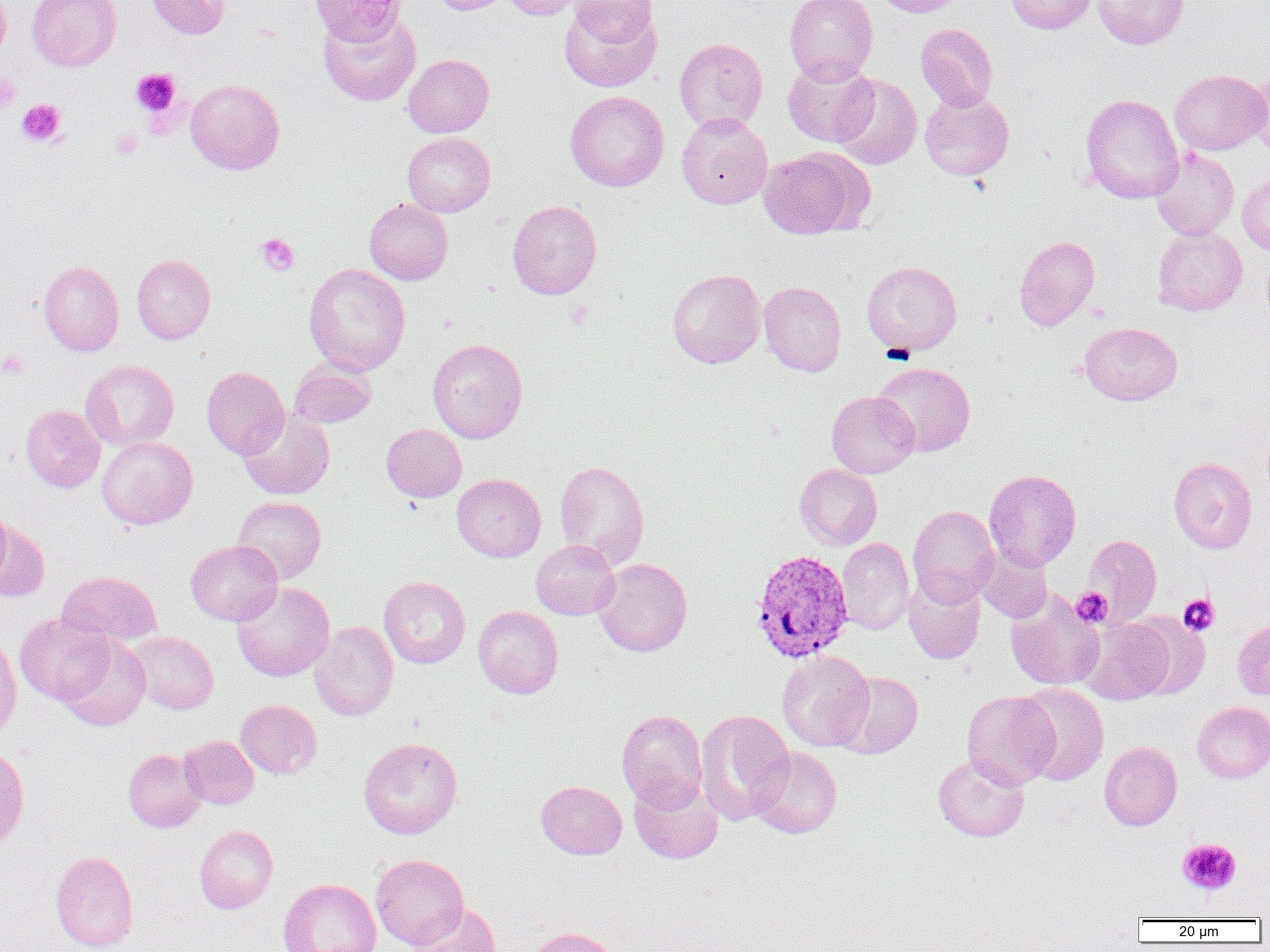

Summary:
  - Coordinate format: approximate bounding boxes as [x1, y1, x2, y2] in pixels
  - Uninfected red blood cell locations: [0, 0, 10, 68], [26, 0, 122, 71], [147, 0, 231, 39], [309, 0, 404, 46], [429, 0, 511, 15], [501, 0, 595, 21], [785, 0, 878, 85], [873, 0, 967, 17], [1004, 0, 1097, 34], [1093, 0, 1189, 49], [559, 1, 662, 93], [565, 1, 660, 45], [318, 10, 421, 106], [916, 23, 998, 111], [674, 38, 767, 132], [403, 54, 494, 137], [783, 59, 878, 147], [1246, 65, 1270, 159], [1169, 69, 1269, 155], [833, 74, 922, 170], [185, 79, 284, 175], [920, 90, 1014, 181], [565, 91, 669, 192], [1080, 93, 1183, 204], [676, 112, 773, 209], [401, 132, 495, 217], [757, 147, 870, 239], [1150, 148, 1239, 240], [1237, 174, 1270, 255], [364, 198, 453, 285], [507, 200, 601, 300], [1153, 226, 1247, 316], [1013, 236, 1099, 331], [1261, 251, 1270, 330], [132, 254, 215, 344], [862, 260, 962, 356], [38, 261, 124, 356], [304, 263, 410, 376], [667, 268, 765, 369], [759, 281, 847, 376], [1079, 322, 1182, 406], [427, 338, 527, 443], [80, 360, 179, 451], [288, 360, 377, 428], [872, 362, 976, 457], [201, 366, 289, 459], [826, 391, 920, 478], [21, 405, 105, 493], [238, 408, 335, 500], [381, 424, 467, 502], [97, 436, 198, 529], [1169, 457, 1257, 554], [554, 460, 649, 568], [795, 464, 882, 550], [984, 469, 1081, 570], [451, 473, 546, 562], [232, 496, 326, 585], [0, 504, 13, 590], [908, 505, 999, 605], [0, 521, 50, 602], [1083, 534, 1162, 626], [837, 537, 914, 634], [186, 540, 282, 625], [531, 540, 619, 620], [974, 545, 1053, 623], [593, 558, 692, 657], [57, 570, 163, 647], [903, 572, 986, 665], [379, 576, 470, 669], [232, 582, 334, 681], [1005, 590, 1105, 691], [473, 605, 563, 699], [15, 613, 115, 705], [1126, 613, 1211, 699], [1078, 618, 1173, 705], [1233, 619, 1270, 702], [310, 621, 398, 722], [126, 631, 218, 714], [57, 634, 151, 731], [0, 635, 21, 742], [777, 650, 875, 751], [834, 671, 923, 758], [1016, 683, 1109, 786], [962, 690, 1060, 789], [235, 699, 322, 779], [1192, 701, 1270, 782], [616, 709, 708, 810], [695, 709, 794, 824], [178, 736, 258, 809], [358, 737, 462, 839], [1099, 740, 1182, 831], [0, 744, 30, 851], [749, 747, 842, 838], [123, 749, 205, 832], [932, 752, 1030, 842], [629, 776, 724, 864], [536, 780, 627, 859], [194, 824, 278, 913], [51, 850, 138, 952], [371, 853, 468, 950], [278, 878, 381, 952], [408, 902, 503, 952], [524, 926, 620, 952]
  - Platelet locations: [130, 68, 181, 118], [0, 72, 21, 115], [16, 99, 66, 147], [110, 128, 142, 159], [256, 233, 299, 276], [566, 301, 593, 330], [0, 350, 30, 379], [1071, 587, 1112, 627], [1178, 594, 1220, 636], [1177, 838, 1242, 895]
  - Plasmodium vivax-infected red blood cell locations: [750, 548, 854, 663]
  - Slide-level diagnosis: Plasmodium vivax
  - Preparation: thin blood smear
  - Modality: light microscopy
  - Field of view: single
  - Magnification: 1000x
  - Image size: 1270×952 pixels